Classify this cell by malaria status.
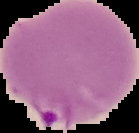
It is parasitized.

Summary:
  - Image type: cell region segmented out of the field of view; surrounding area masked to black
  - Image size: 139×133 pixels
  - Preparation: thin blood film